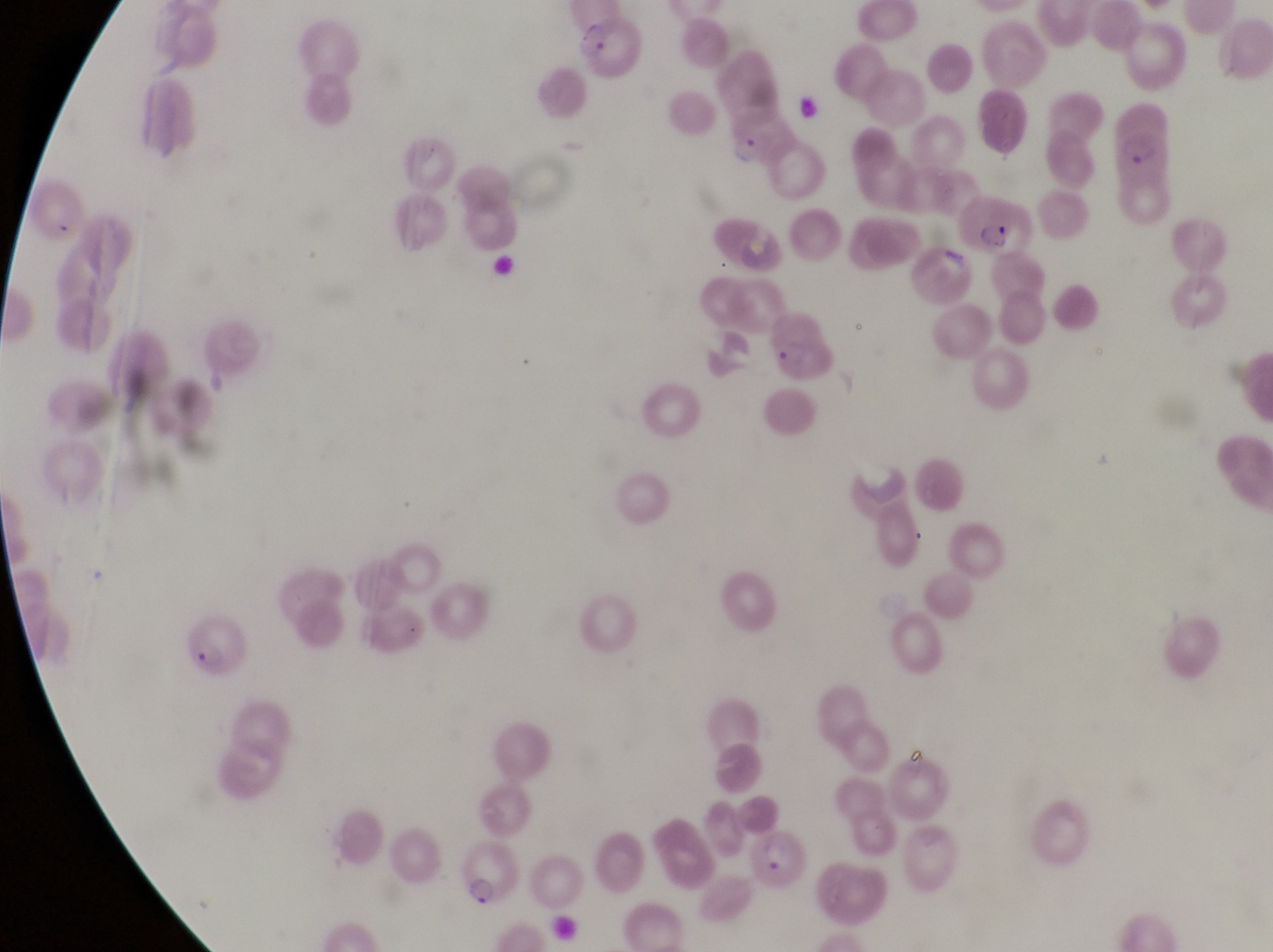
Approximate bounding boxes as {left, top, right, bottom} in pixels.
Summary:
  - Trophozoite locations: {731, 132, 766, 171}
  - Parasitised red blood cell locations: {579, 17, 649, 82}, {1117, 108, 1177, 186}, {964, 190, 1034, 262}, {768, 309, 842, 389}, {177, 617, 251, 679}, {752, 829, 814, 896}, {460, 839, 525, 917}
  - Preparation: thin blood smear
  - Field of view: single
  - Magnification: 1000x
  - Capture: smartphone photograph through the eyepiece of an Olympus CX-23 microscope
  - Country: Uganda
  - Image size: 1273×952 pixels